Identify the preparation type.
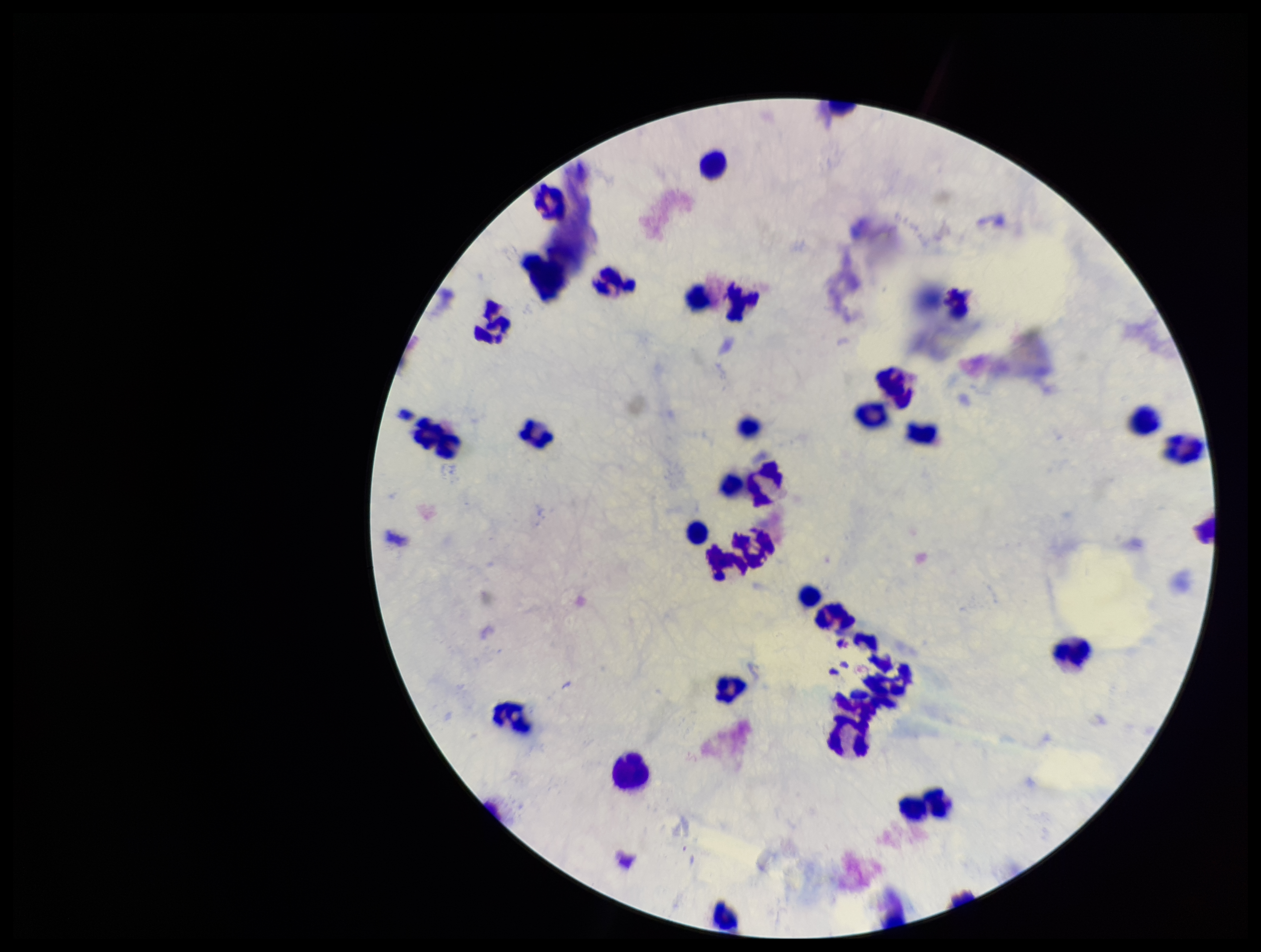

A thick smear.

Parasite count: 0. Single field of view. Image is 1261×952 pixels. Plasmodium parasites: none identified. Giemsa stain. Photographed through the microscope eyepiece with a smartphone camera. Leukocyte count: 34. Patient malaria status: negative.